Locate every blood parasite and identify its species.
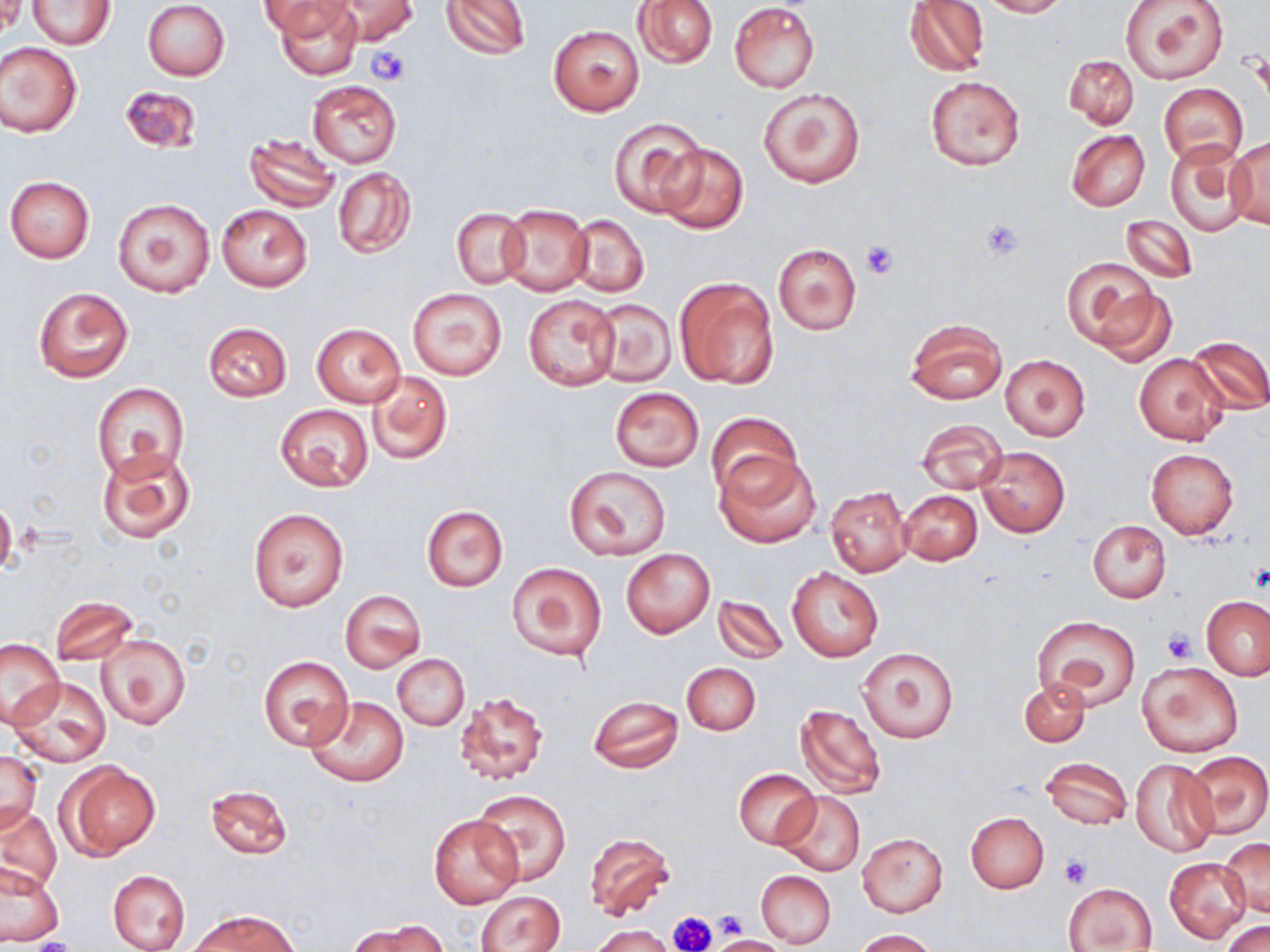
No blood parasites seen.

Summary:
  - Coordinate format: approximate bounding boxes as (x1,y1)-(x2,y2) corner pairs in pixels
  - Platelet locations: (367,47)-(409,84), (981,218)-(1025,259), (859,239)-(899,279), (1246,564)-(1269,593), (1162,628)-(1197,663), (1060,856)-(1092,886), (713,908)-(748,940), (669,910)-(717,951), (24,938)-(79,952)
  - Uninfected red blood cell locations: (1,0)-(25,37), (329,0)-(419,45), (441,0)-(531,60), (634,0)-(718,68), (979,0)-(1067,18), (1119,0)-(1229,85), (30,1)-(114,49), (143,1)-(230,81), (262,1)-(353,39), (272,1)-(363,80), (904,1)-(990,76), (729,3)-(821,92), (548,25)-(644,116), (0,43)-(82,137), (1063,55)-(1139,129), (925,76)-(1026,170), (307,80)-(402,168), (1158,83)-(1248,167), (119,85)-(202,155), (758,86)-(867,189), (608,116)-(705,216), (1067,129)-(1150,211), (243,133)-(340,212), (1226,136)-(1270,230), (655,142)-(748,234), (1167,143)-(1252,234), (333,167)-(416,258), (5,176)-(95,262), (113,198)-(215,298), (216,204)-(311,292), (498,204)-(593,296), (452,208)-(529,288), (568,214)-(649,296), (1119,215)-(1197,284), (773,243)-(861,335), (1061,257)-(1164,351), (674,277)-(780,390), (33,286)-(133,383), (1093,286)-(1176,366), (408,287)-(507,381), (523,294)-(620,392), (589,297)-(676,388), (905,318)-(1008,406), (203,322)-(291,402), (311,322)-(407,408), (1187,335)-(1270,415), (1001,354)-(1090,440), (1135,355)-(1229,445), (365,370)-(453,465), (93,382)-(188,481), (608,387)-(704,472), (275,405)-(374,492), (704,412)-(802,505), (916,418)-(1009,495), (976,445)-(1070,537), (98,448)-(197,543), (1146,449)-(1238,540), (715,450)-(821,549), (564,466)-(668,561), (825,484)-(913,576), (899,490)-(982,565), (0,501)-(17,576), (421,506)-(508,592), (248,507)-(348,611), (1088,520)-(1172,603), (621,549)-(715,638), (506,560)-(608,664), (786,566)-(883,662), (340,590)-(425,672), (713,596)-(787,663), (1203,596)-(1269,680), (49,597)-(138,666), (1033,616)-(1141,709), (97,632)-(190,730), (0,638)-(64,727), (858,647)-(958,744), (258,654)-(353,750), (393,655)-(470,730), (1138,661)-(1243,758), (682,662)-(761,735), (10,676)-(111,767), (1018,678)-(1089,747), (452,689)-(550,789), (588,695)-(683,773), (305,696)-(410,786), (792,703)-(887,800), (0,751)-(43,835), (1183,751)-(1270,839), (1041,756)-(1132,830), (1130,758)-(1219,858), (60,762)-(161,860), (734,768)-(819,849), (205,785)-(292,859), (474,788)-(571,884), (777,791)-(867,877), (0,806)-(63,895), (429,812)-(524,909), (965,812)-(1049,893), (584,832)-(675,919), (858,833)-(948,916), (1222,838)-(1270,916), (1166,857)-(1251,944), (0,863)-(64,944), (107,869)-(191,952), (756,870)-(836,948), (1064,882)-(1157,951), (477,891)-(566,952), (189,910)-(298,952), (354,919)-(448,952), (1223,920)-(1270,952), (593,925)-(675,952), (853,929)-(937,952), (709,934)-(785,952)
  - Slide-level diagnosis: negative for blood parasites
  - Field of view: single
  - Image size: 1270×952 pixels
  - Preparation: thin blood film
  - Stain: May-Grünwald-Giemsa
  - Modality: light microscopy
  - Magnification: 1000x